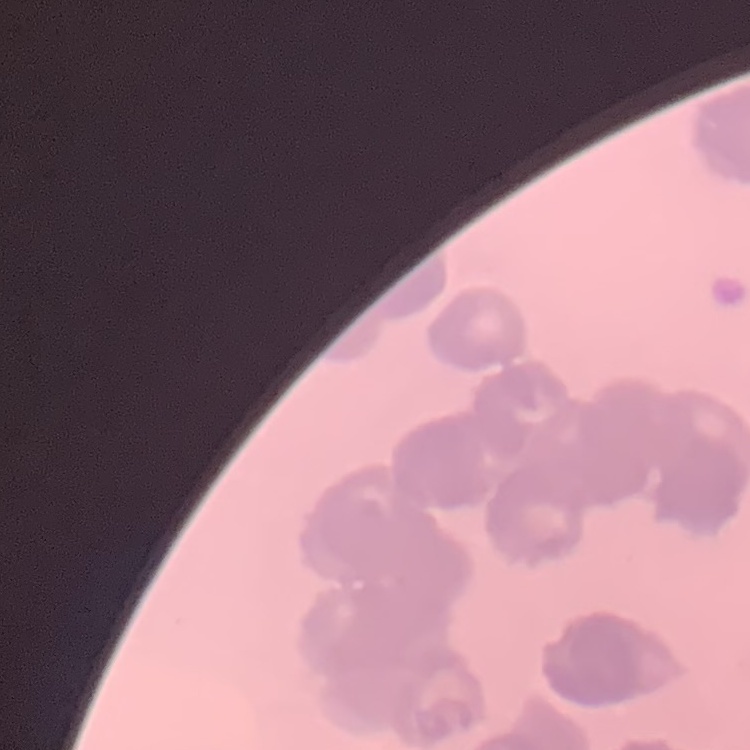

erythrocyte morphology = rouleaux formation
image type = square crop of a larger photomicrograph
stain = Field's or Giemsa
preparation = thin peripheral smear